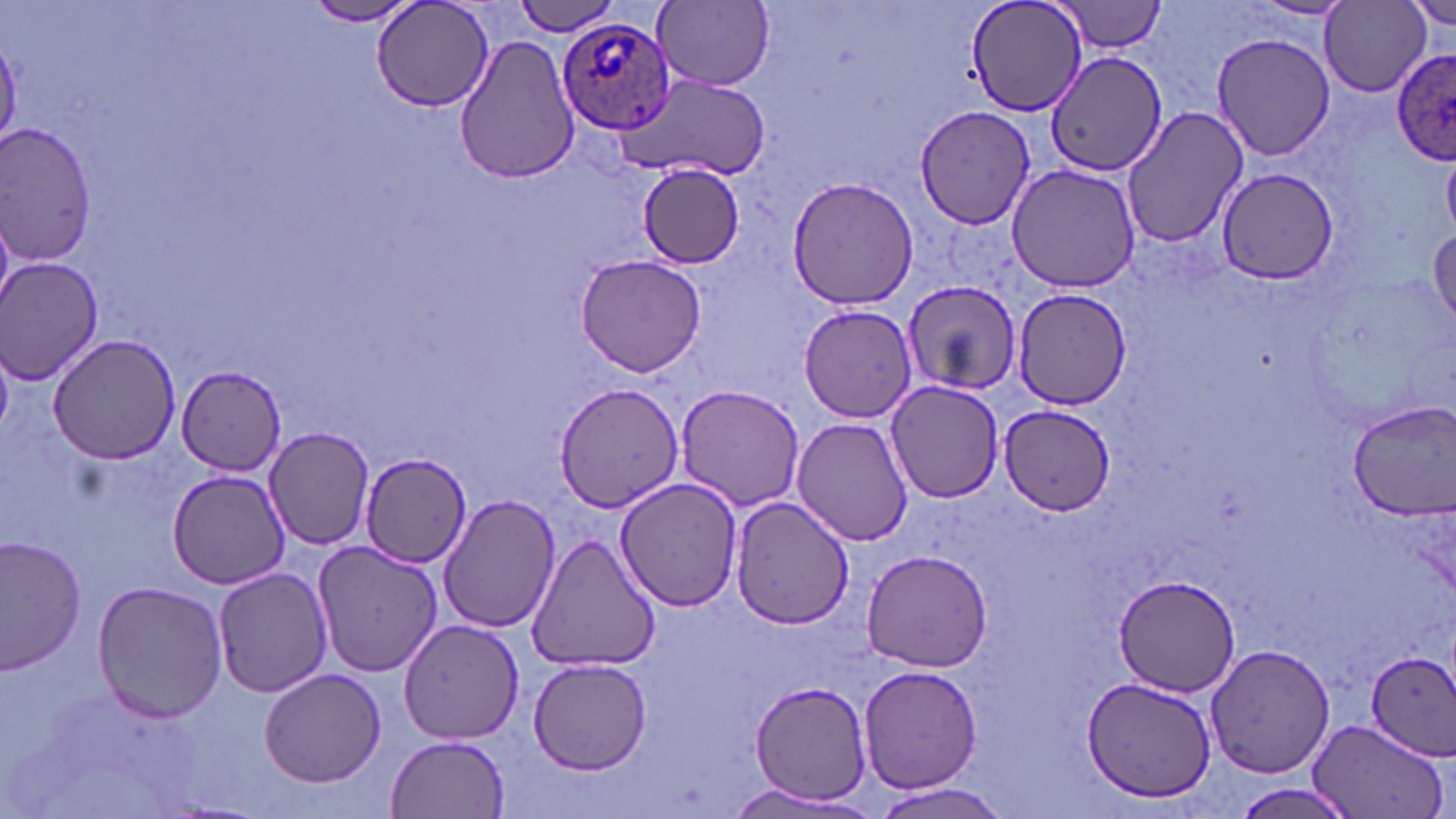

slide-level diagnosis = Plasmodium ovale
magnification = 1000x
image size = 1456×819 pixels
uninfected red blood cell locations = approximate bounding boxes as named x1/y1/x2/y2 corners in pixels: (x1=301, y1=0, x2=422, y2=26), (x1=372, y1=0, x2=495, y2=114), (x1=964, y1=0, x2=1091, y2=119), (x1=1249, y1=0, x2=1354, y2=20), (x1=1402, y1=0, x2=1456, y2=28), (x1=509, y1=1, x2=621, y2=37), (x1=655, y1=1, x2=776, y2=90), (x1=1051, y1=1, x2=1169, y2=54), (x1=1321, y1=2, x2=1431, y2=95), (x1=1211, y1=30, x2=1336, y2=162), (x1=452, y1=33, x2=583, y2=184), (x1=0, y1=38, x2=24, y2=145), (x1=1045, y1=51, x2=1167, y2=177), (x1=615, y1=75, x2=771, y2=179), (x1=915, y1=104, x2=1037, y2=231), (x1=1122, y1=106, x2=1247, y2=250), (x1=0, y1=125, x2=97, y2=264), (x1=1445, y1=155, x2=1456, y2=235), (x1=638, y1=163, x2=746, y2=268), (x1=1007, y1=164, x2=1139, y2=293), (x1=1214, y1=170, x2=1342, y2=286), (x1=786, y1=176, x2=917, y2=309), (x1=1429, y1=224, x2=1456, y2=332), (x1=573, y1=253, x2=709, y2=377), (x1=0, y1=258, x2=105, y2=385), (x1=903, y1=282, x2=1020, y2=396), (x1=1010, y1=287, x2=1133, y2=408), (x1=798, y1=304, x2=919, y2=423), (x1=49, y1=334, x2=180, y2=464), (x1=174, y1=363, x2=289, y2=476), (x1=884, y1=379, x2=1005, y2=502), (x1=554, y1=381, x2=687, y2=515), (x1=673, y1=385, x2=806, y2=512), (x1=1344, y1=398, x2=1456, y2=518), (x1=999, y1=406, x2=1116, y2=513), (x1=792, y1=417, x2=914, y2=545), (x1=264, y1=426, x2=373, y2=550), (x1=361, y1=458, x2=471, y2=567), (x1=167, y1=469, x2=292, y2=588), (x1=614, y1=478, x2=744, y2=612), (x1=438, y1=494, x2=562, y2=633), (x1=731, y1=496, x2=856, y2=629), (x1=525, y1=533, x2=660, y2=672), (x1=0, y1=534, x2=87, y2=674), (x1=309, y1=540, x2=444, y2=678), (x1=862, y1=549, x2=992, y2=671), (x1=214, y1=568, x2=334, y2=698), (x1=1113, y1=574, x2=1243, y2=694), (x1=90, y1=581, x2=228, y2=723), (x1=399, y1=618, x2=523, y2=744), (x1=1205, y1=642, x2=1333, y2=778), (x1=1365, y1=649, x2=1456, y2=761), (x1=528, y1=657, x2=653, y2=774), (x1=859, y1=664, x2=983, y2=792), (x1=261, y1=668, x2=385, y2=786), (x1=1083, y1=675, x2=1218, y2=803), (x1=749, y1=679, x2=877, y2=803), (x1=1305, y1=719, x2=1447, y2=819), (x1=387, y1=735, x2=510, y2=816), (x1=867, y1=780, x2=1014, y2=816), (x1=721, y1=782, x2=868, y2=814)
field of view = one of a larger specimen
preparation = thin blood film
modality = light microscopy
stain = May-Grünwald-Giemsa
Plasmodium ovale-infected red blood cell locations = approximate bounding boxes as named x1/y1/x2/y2 corners in pixels: (x1=556, y1=20, x2=675, y2=134), (x1=1392, y1=46, x2=1455, y2=166)